Assess the background quality.
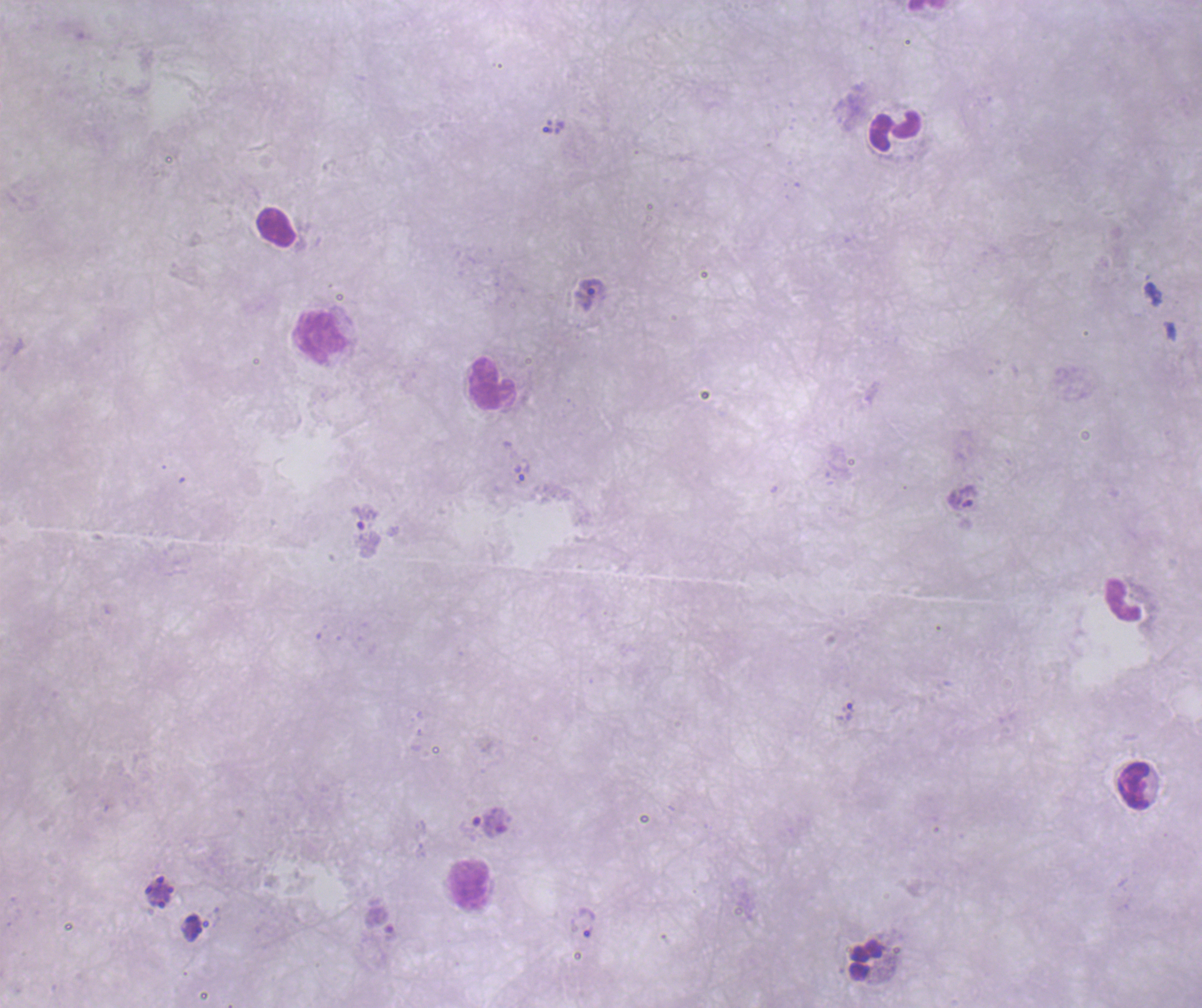

It is poor.

coordinate format = approximate centers as [x, y] in pixels
leukocyte locations = [896, 131], [276, 227], [320, 337], [492, 383], [1123, 600], [1133, 785], [470, 884], [865, 960]
trophozoite locations = [590, 294], [521, 472], [365, 517], [844, 712], [586, 921]
context = previously used in a real diagnosis
field of view = single
image size = 1202×1008 pixels
magnification = 100x
stain = Romanowsky
result = malaria parasites detected
coloration quality = bad
preparation = thick blood smear